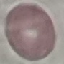

{
  "result": "no malaria parasites detected",
  "stain": "Giemsa",
  "capture": "smartphone camera at the microscope eyepiece",
  "preparation": "thin blood smear",
  "image_type": "automatically extracted cell patch, resized to 64 × 64 pixels"
}